Locate platelets.
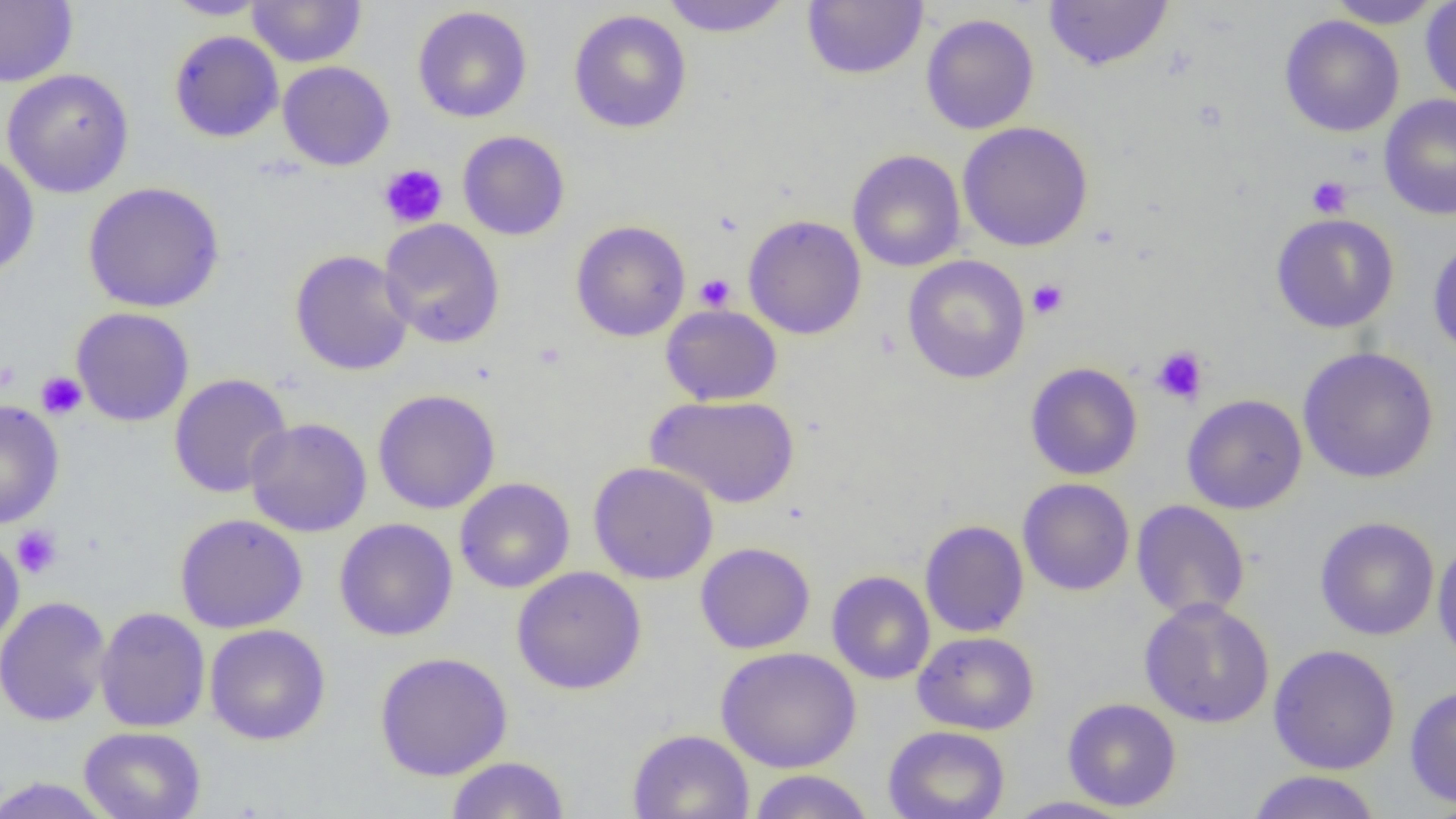
Approximate bounding boxes as named x1/y1/x2/y2 corners in pixels.
Platelets: (x1=379, y1=163, x2=448, y2=228), (x1=1307, y1=176, x2=1352, y2=218), (x1=694, y1=273, x2=736, y2=311), (x1=1027, y1=278, x2=1069, y2=320), (x1=1151, y1=346, x2=1208, y2=405), (x1=0, y1=361, x2=21, y2=393), (x1=36, y1=371, x2=87, y2=420), (x1=11, y1=525, x2=63, y2=578).

slide_level_diagnosis: no evidence of blood parasites
field_of_view: single
image_size: 1456×819 pixels
modality: optical microscopy
magnification: 1000x
preparation: thin blood film
uninfected_red_blood_cell_locations: 'approximate bounding boxes as named x1/y1/x2/y2 corners in pixels: (x1=0, y1=0, x2=78, y2=86), (x1=163, y1=0, x2=271, y2=20), (x1=248, y1=0, x2=367, y2=67), (x1=659, y1=0, x2=794, y2=37), (x1=802, y1=0, x2=928, y2=80), (x1=1043, y1=0, x2=1173, y2=72), (x1=1326, y1=0, x2=1445, y2=29), (x1=1421, y1=0, x2=1456, y2=105), (x1=413, y1=5, x2=533, y2=123), (x1=568, y1=9, x2=692, y2=134), (x1=920, y1=13, x2=1039, y2=134), (x1=1279, y1=15, x2=1405, y2=137), (x1=169, y1=30, x2=284, y2=143), (x1=277, y1=61, x2=395, y2=171), (x1=1, y1=68, x2=135, y2=198), (x1=1379, y1=93, x2=1456, y2=221), (x1=957, y1=121, x2=1093, y2=251), (x1=457, y1=130, x2=570, y2=241), (x1=847, y1=149, x2=966, y2=272), (x1=0, y1=153, x2=39, y2=279), (x1=83, y1=181, x2=224, y2=313), (x1=1270, y1=213, x2=1399, y2=333), (x1=742, y1=214, x2=867, y2=340), (x1=379, y1=218, x2=505, y2=348), (x1=570, y1=220, x2=690, y2=342), (x1=1428, y1=237, x2=1456, y2=360), (x1=290, y1=249, x2=415, y2=376), (x1=902, y1=254, x2=1030, y2=384), (x1=661, y1=304, x2=782, y2=405), (x1=71, y1=307, x2=194, y2=427), (x1=1298, y1=346, x2=1439, y2=484), (x1=1025, y1=362, x2=1143, y2=480), (x1=168, y1=373, x2=293, y2=498), (x1=373, y1=389, x2=500, y2=514), (x1=645, y1=394, x2=800, y2=508), (x1=1182, y1=394, x2=1308, y2=514), (x1=0, y1=400, x2=65, y2=528), (x1=245, y1=417, x2=372, y2=537), (x1=588, y1=461, x2=718, y2=584), (x1=454, y1=478, x2=574, y2=594), (x1=1017, y1=478, x2=1134, y2=596), (x1=1131, y1=500, x2=1250, y2=622), (x1=174, y1=513, x2=307, y2=634), (x1=1315, y1=516, x2=1440, y2=641), (x1=334, y1=518, x2=458, y2=641), (x1=919, y1=519, x2=1029, y2=637), (x1=0, y1=534, x2=25, y2=651), (x1=1432, y1=539, x2=1456, y2=669), (x1=695, y1=542, x2=815, y2=654), (x1=511, y1=566, x2=647, y2=695), (x1=827, y1=571, x2=935, y2=684), (x1=0, y1=596, x2=112, y2=727), (x1=1139, y1=597, x2=1275, y2=728), (x1=95, y1=607, x2=211, y2=733), (x1=204, y1=624, x2=331, y2=745), (x1=913, y1=631, x2=1039, y2=735), (x1=1268, y1=644, x2=1401, y2=775), (x1=716, y1=646, x2=861, y2=772), (x1=375, y1=651, x2=513, y2=781), (x1=1405, y1=684, x2=1456, y2=809), (x1=1063, y1=698, x2=1181, y2=811), (x1=78, y1=726, x2=206, y2=819), (x1=883, y1=726, x2=1010, y2=819), (x1=628, y1=728, x2=754, y2=818), (x1=446, y1=756, x2=569, y2=818), (x1=746, y1=769, x2=875, y2=818), (x1=1246, y1=770, x2=1382, y2=819), (x1=0, y1=776, x2=116, y2=818), (x1=1002, y1=795, x2=1137, y2=818)'